Point out each malaria parasite and each leukocyte.
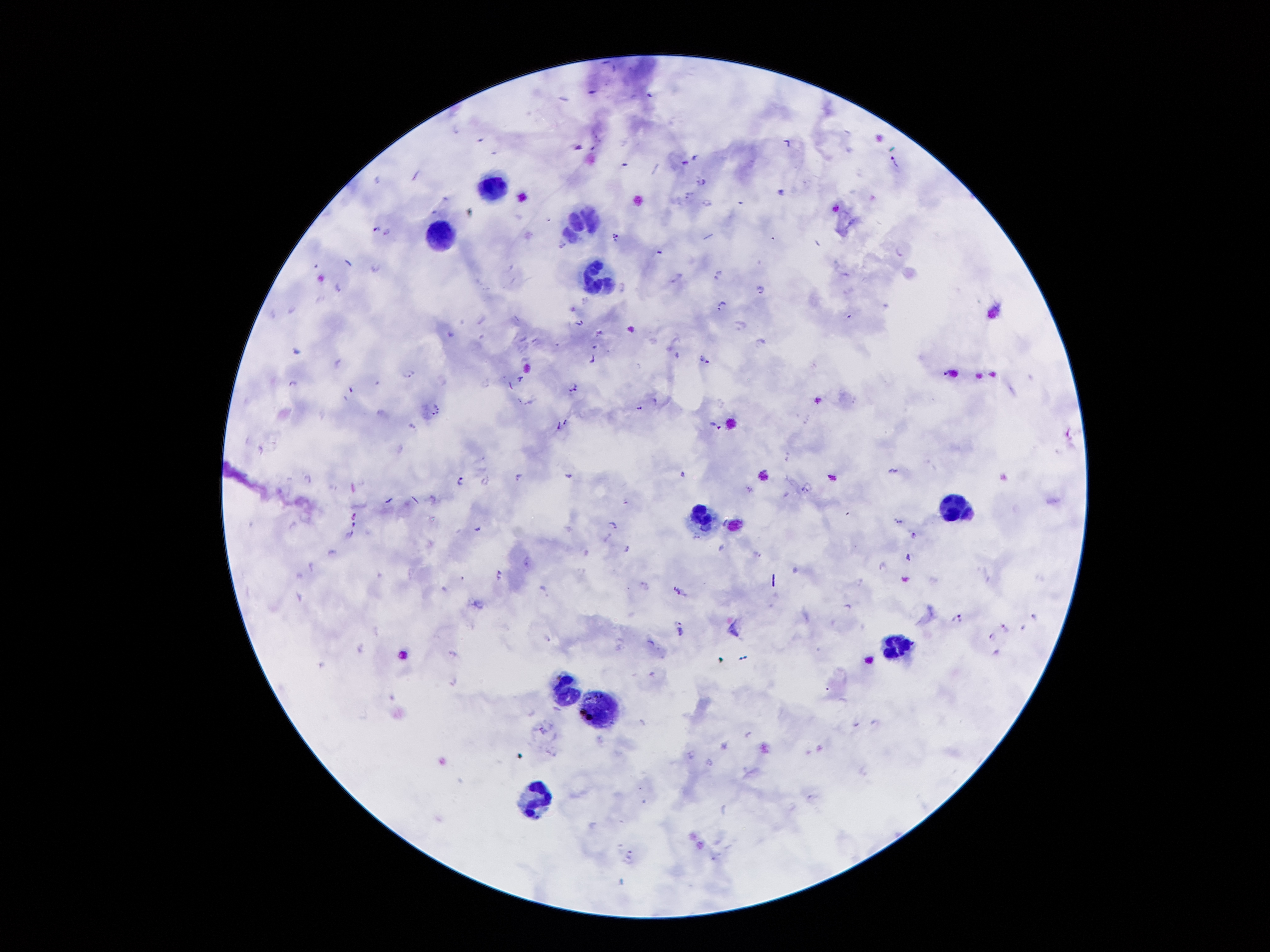
Approximate centers as (x, y) in pixels.
Malaria parasites: (893, 160), (701, 181), (781, 191), (687, 194), (709, 202), (375, 226), (387, 233), (615, 237), (562, 243), (374, 268), (718, 274), (677, 278), (338, 286), (761, 288), (719, 303), (580, 322), (738, 325), (599, 333), (537, 341), (761, 344), (677, 354), (592, 359), (705, 360), (336, 362), (408, 372), (520, 378), (293, 381), (511, 385), (573, 387), (351, 392), (519, 400), (436, 407), (640, 408), (566, 421), (715, 424), (558, 426), (259, 447), (892, 470), (683, 474), (568, 475), (518, 476), (306, 478), (460, 480), (485, 480), (806, 487), (749, 491), (434, 496), (354, 515), (898, 521), (352, 522), (613, 525), (476, 528), (350, 534), (914, 535), (627, 549), (909, 556), (882, 565), (498, 574), (643, 584), (678, 590), (1032, 615), (957, 616), (677, 621), (1004, 627), (680, 633), (990, 636), (997, 651), (452, 653), (452, 679), (542, 730), (750, 735), (690, 753), (810, 798), (628, 851), (627, 861).
Leukocytes: (493, 190), (586, 219), (441, 235), (596, 275), (954, 512), (698, 515), (895, 647), (566, 689), (603, 714), (535, 798).

Summary:
  - Capture: smartphone camera through the microscope eyepiece
  - Patient malaria status: positive for Plasmodium falciparum
  - Preparation: thick blood smear
  - Magnification: 100x
  - Field of view: one from this slide
  - Image size: 1270×952 pixels
  - Stain: Giemsa